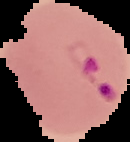

result = Plasmodium parasites detected
image size = 130×142 pixels
image type = cell region segmented out of the field of view; surrounding area masked to black
preparation = thin blood film